Give a bounding box for every leukocyte visible.
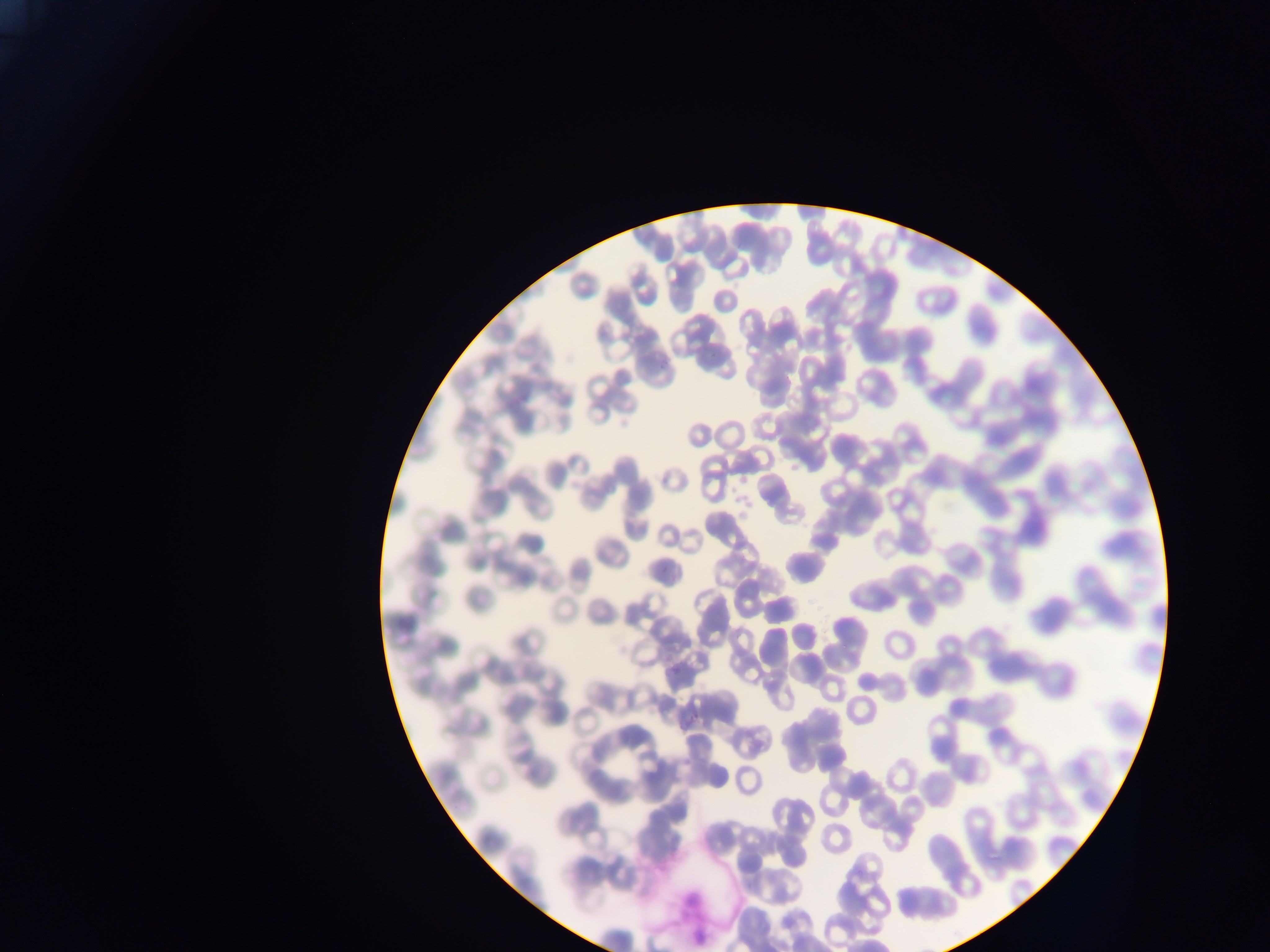

No leukocytes observed.

Approximate bounding boxes as (left, top, right, bottom) in pixels. Artifact (stain precipitate or debris) locations: (676, 883, 715, 943). Plasmodium parasite locations: (689, 714, 700, 723), (856, 867, 865, 875) | approximate (x, y) pixel centers of objects too small to bound: (663, 366). Thin blood smear. Mobile-phone photograph taken through the microscope. Sample from Ghana. Single field of view. Image is 1270×952 pixels.